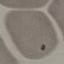

Malaria status: uninfected. Acquired by smartphone through the microscope eyepiece. Giemsa stain. Thin blood film. Cell patch, automatically extracted from a larger field of view and resized to 64 × 64 pixels.